Classify this cell by malaria status.
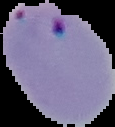
Parasitized.

preparation = thin blood smear
image size = 115×127 pixels
image type = segmented cell region with the area outside set to black